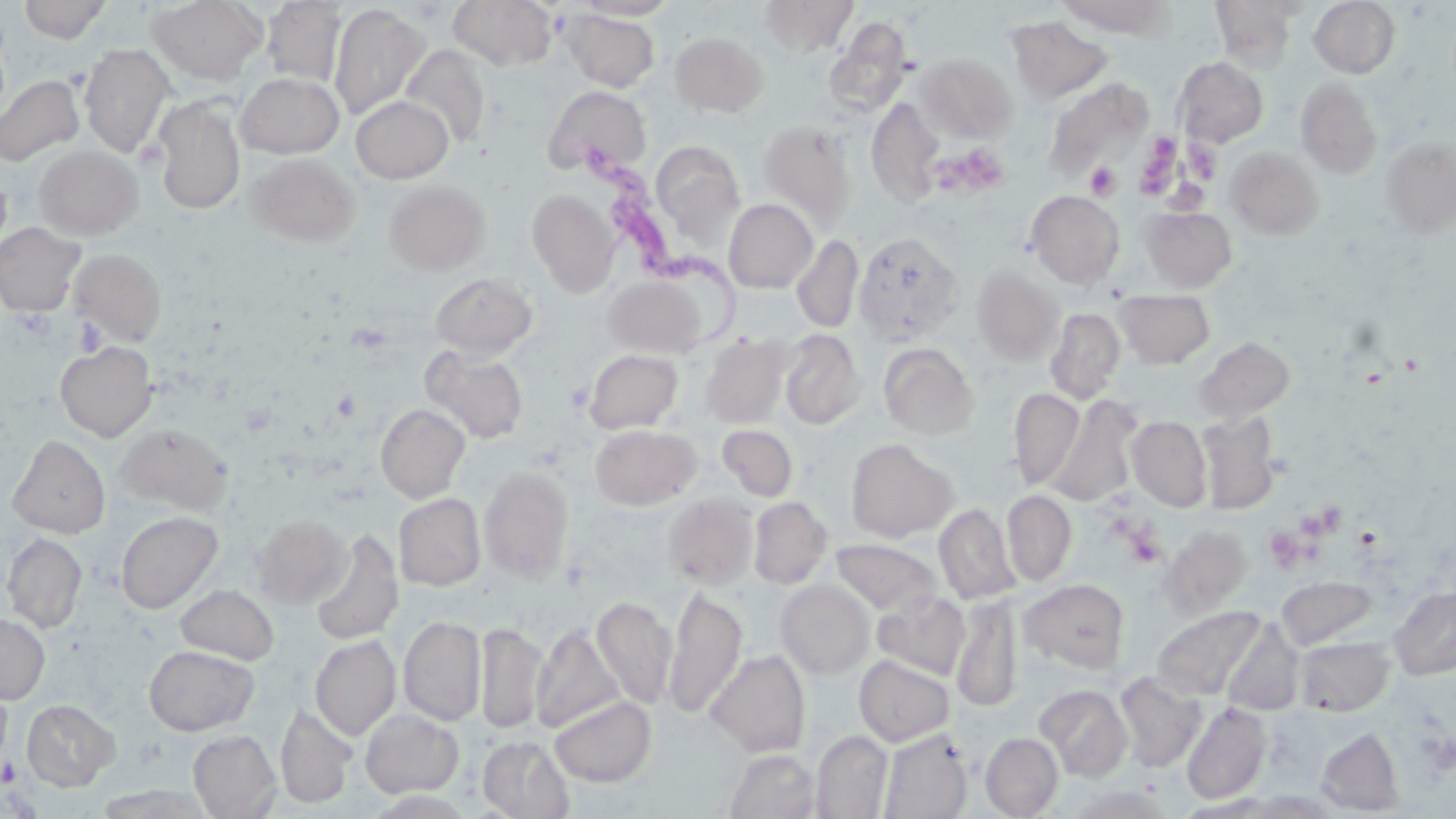
slide-level diagnosis = Trypanosoma brucei
uninfected red blood cell locations = approximate bounding boxes as (x1,y1)-(x2,y2) corner pairs in pixels: (18,0)-(110,43), (147,0)-(266,85), (448,0)-(557,70), (573,0)-(680,20), (759,0)-(859,57), (1054,0)-(1176,38), (1210,0)-(1300,71), (1309,0)-(1400,78), (261,1)-(347,87), (328,3)-(430,120), (561,9)-(659,92), (1006,16)-(1111,103), (823,18)-(913,119), (670,31)-(769,116), (79,44)-(175,157), (400,44)-(491,149), (915,52)-(1017,143), (1173,56)-(1268,148), (234,72)-(345,158), (0,74)-(84,166), (1295,78)-(1383,179), (1045,79)-(1152,181), (544,85)-(651,177), (352,96)-(453,183), (153,97)-(245,215), (866,97)-(945,207), (758,120)-(857,230), (1381,136)-(1456,237), (651,140)-(745,244), (34,145)-(143,240), (1226,147)-(1323,240), (246,152)-(360,247), (384,180)-(489,274), (527,188)-(620,296), (1025,190)-(1125,289), (724,199)-(817,293), (1140,206)-(1236,292), (0,223)-(85,316), (853,231)-(963,345), (791,234)-(864,334), (69,248)-(167,346), (972,265)-(1065,365), (430,272)-(537,358), (604,276)-(704,357), (1114,289)-(1215,368), (1044,308)-(1126,404), (780,329)-(864,429), (701,335)-(790,427), (1195,336)-(1294,424), (55,341)-(157,441), (878,343)-(979,440), (421,346)-(528,444), (584,349)-(683,434), (1008,388)-(1085,490), (1046,395)-(1141,507), (376,404)-(470,502), (1196,412)-(1282,514), (1127,416)-(1212,511), (115,422)-(234,516), (590,424)-(701,510), (717,424)-(798,501), (8,434)-(110,538), (845,438)-(957,542), (479,465)-(574,583), (1002,491)-(1077,586), (394,493)-(485,590), (663,494)-(758,589), (749,496)-(832,588), (934,503)-(1019,605), (116,511)-(222,613), (251,513)-(351,609), (1158,526)-(1254,619), (309,530)-(404,646), (1,533)-(87,632), (830,539)-(942,616), (1277,575)-(1379,650), (776,579)-(875,678), (1020,579)-(1130,672), (176,584)-(279,665), (1389,584)-(1456,680), (665,588)-(746,718), (873,591)-(970,679), (952,593)-(1022,713), (591,596)-(676,709), (1151,606)-(1266,700), (0,612)-(50,704), (398,616)-(486,726), (474,622)-(547,734), (531,624)-(624,733), (310,635)-(401,740), (1295,636)-(1394,716), (144,645)-(258,736), (706,649)-(811,758), (854,654)-(955,746), (1115,671)-(1206,772), (1035,684)-(1133,782), (549,696)-(656,786), (22,699)-(120,790), (1181,702)-(1271,805), (275,703)-(356,809), (360,709)-(464,798), (1317,727)-(1405,815), (878,729)-(972,819), (188,730)-(281,818), (812,730)-(893,818), (980,732)-(1064,818), (478,736)-(574,818), (725,749)-(821,819)
magnification = 1000x
Trypanosoma brucei locations = approximate bounding boxes as (x1,y1)-(x2,y2) corner pairs in pixels: (587,143)-(759,352)
preparation = thin blood film
field of view = single
modality = light microscopy
image size = 1456×819 pixels
platelet locations = approximate bounding boxes as (x1,y1)-(x2,y2) corner pairs in pixels: (1137,136)-(1182,193), (137,141)-(166,170), (932,143)-(1016,203), (1184,143)-(1221,184), (1085,162)-(1122,201), (75,316)-(105,355), (565,382)-(592,411), (1272,501)-(1351,572), (1122,524)-(1166,569), (2,757)-(19,786)
stain = May-Grünwald-Giemsa